Classify this cell by malaria status.
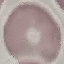

It is uninfected.

Photographed with a smartphone camera at the microscope eyepiece. Thin blood smear. Automatically extracted cell patch, resized to 64 × 64 pixels. Giemsa stain.